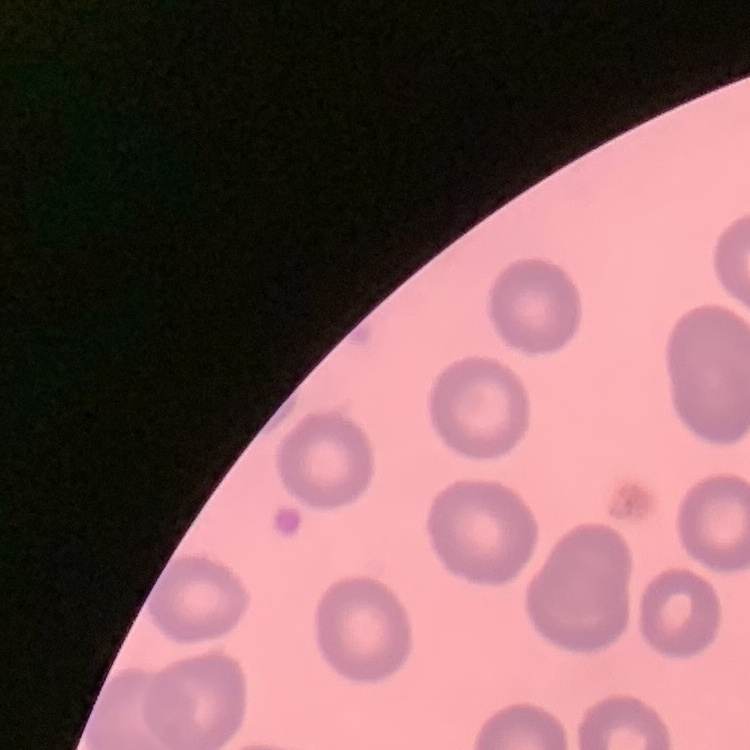

Summary:
  - Erythrocyte morphology: no rouleaux formation
  - Image type: square crop of a larger photomicrograph
  - Preparation: thin blood film
  - Stain: Field's or Giemsa